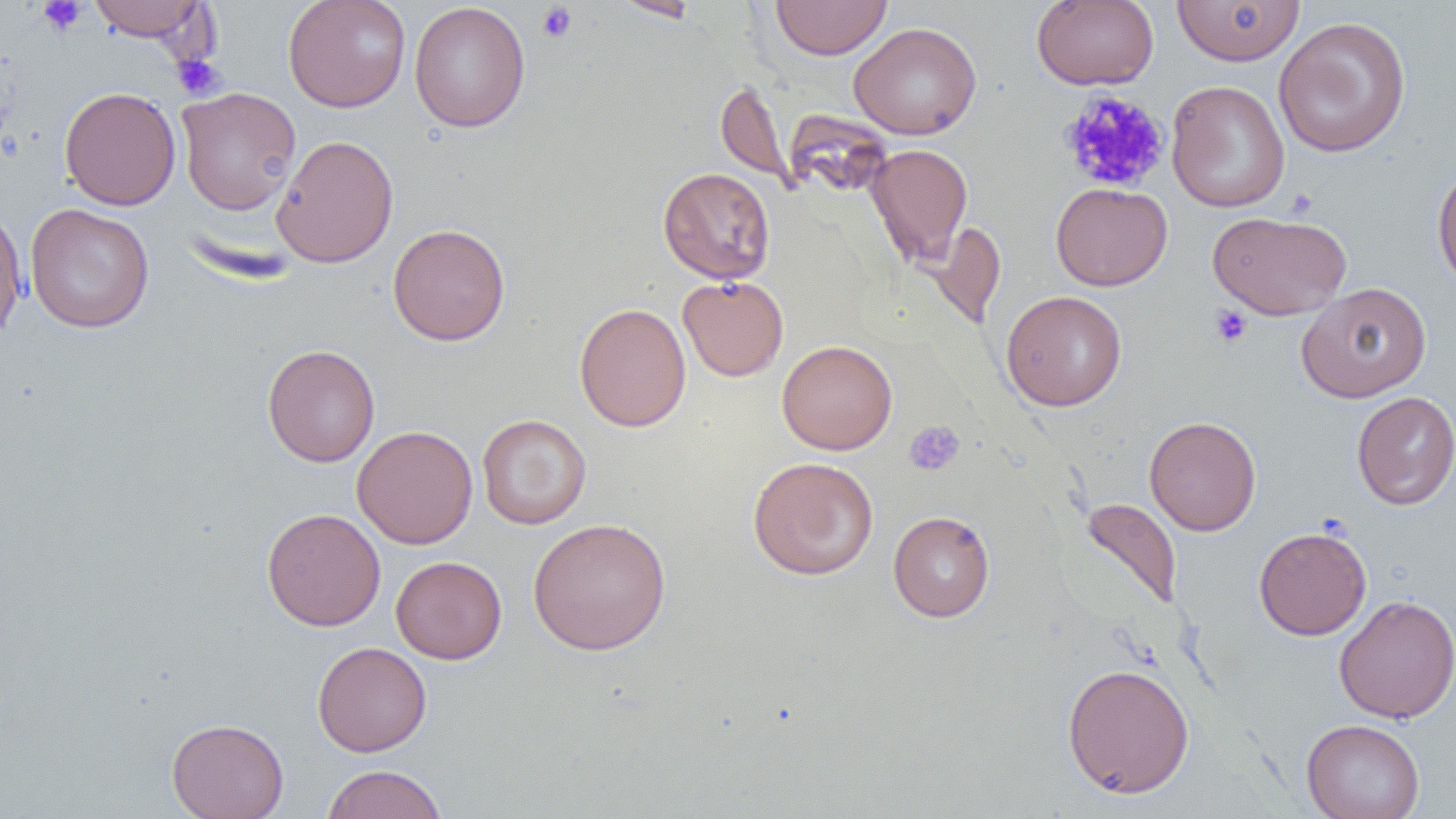
Approximate bounding boxes as named x1/y1/x2/y2 corners in pixels. Uninfected red blood cell locations: (x1=88, y1=0, x2=210, y2=42), (x1=283, y1=0, x2=411, y2=112), (x1=612, y1=0, x2=701, y2=22), (x1=771, y1=0, x2=891, y2=59), (x1=1032, y1=0, x2=1159, y2=90), (x1=1172, y1=1, x2=1305, y2=66), (x1=409, y1=2, x2=530, y2=133), (x1=1273, y1=16, x2=1412, y2=158), (x1=849, y1=21, x2=982, y2=140), (x1=1166, y1=80, x2=1289, y2=213), (x1=715, y1=81, x2=791, y2=189), (x1=59, y1=86, x2=181, y2=210), (x1=176, y1=87, x2=302, y2=216), (x1=272, y1=134, x2=398, y2=268), (x1=865, y1=143, x2=973, y2=267), (x1=1432, y1=164, x2=1456, y2=292), (x1=658, y1=167, x2=776, y2=285), (x1=1051, y1=182, x2=1172, y2=291), (x1=25, y1=203, x2=154, y2=333), (x1=0, y1=204, x2=28, y2=341), (x1=1208, y1=211, x2=1352, y2=320), (x1=927, y1=221, x2=1006, y2=330), (x1=387, y1=223, x2=511, y2=345), (x1=677, y1=275, x2=789, y2=381), (x1=1296, y1=282, x2=1432, y2=402), (x1=1001, y1=290, x2=1127, y2=411), (x1=574, y1=302, x2=691, y2=433), (x1=776, y1=339, x2=897, y2=455), (x1=262, y1=344, x2=381, y2=467), (x1=1351, y1=391, x2=1456, y2=510), (x1=477, y1=414, x2=592, y2=529), (x1=1144, y1=415, x2=1261, y2=535), (x1=352, y1=425, x2=478, y2=549), (x1=748, y1=456, x2=879, y2=580), (x1=1079, y1=497, x2=1183, y2=611), (x1=262, y1=508, x2=386, y2=631), (x1=888, y1=510, x2=995, y2=622), (x1=527, y1=517, x2=671, y2=655), (x1=1253, y1=525, x2=1372, y2=640), (x1=391, y1=556, x2=507, y2=664), (x1=1334, y1=594, x2=1456, y2=724), (x1=312, y1=641, x2=432, y2=757), (x1=1062, y1=662, x2=1195, y2=799), (x1=167, y1=717, x2=289, y2=819), (x1=1301, y1=719, x2=1425, y2=819), (x1=321, y1=764, x2=447, y2=819). Platelet locations: (x1=37, y1=0, x2=88, y2=35), (x1=536, y1=3, x2=577, y2=44), (x1=172, y1=54, x2=225, y2=100), (x1=1059, y1=88, x2=1170, y2=194), (x1=1209, y1=304, x2=1253, y2=348), (x1=904, y1=420, x2=965, y2=476). Slide-level diagnosis: negative for blood parasites. 1000x magnification. Image is 1456×819 pixels. Light microscopy. One field of a larger specimen. Thin blood film.